Describe the morphology of the erythrocytes.
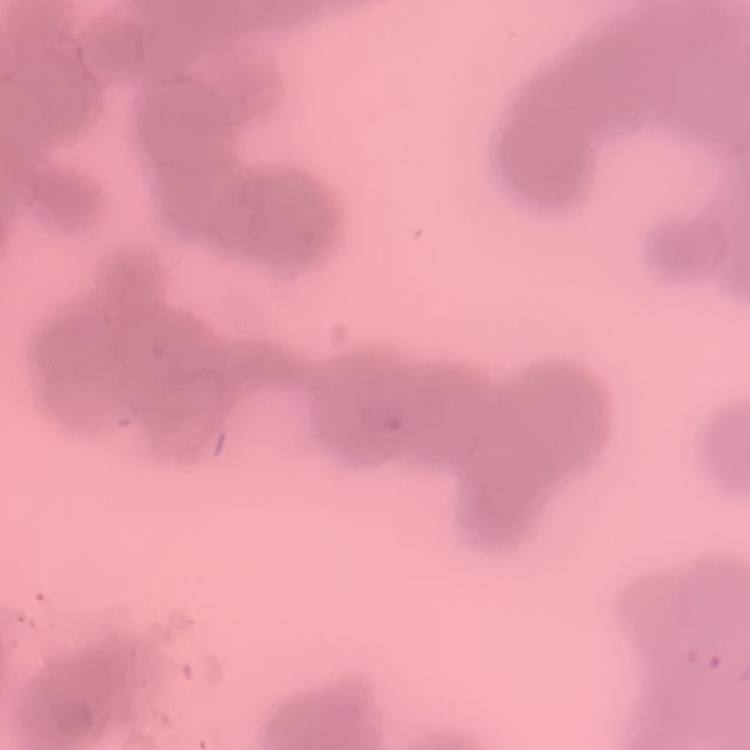

They show rouleaux formation.

Stained with either Field's or Giemsa. Square crop of a larger photomicrograph. Thin peripheral smear.